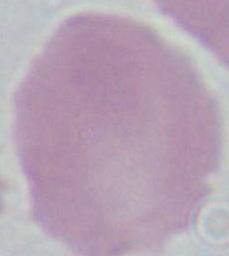
magnification = 1000x
modality = micrograph
identification = red blood cell